Give the preparation type.
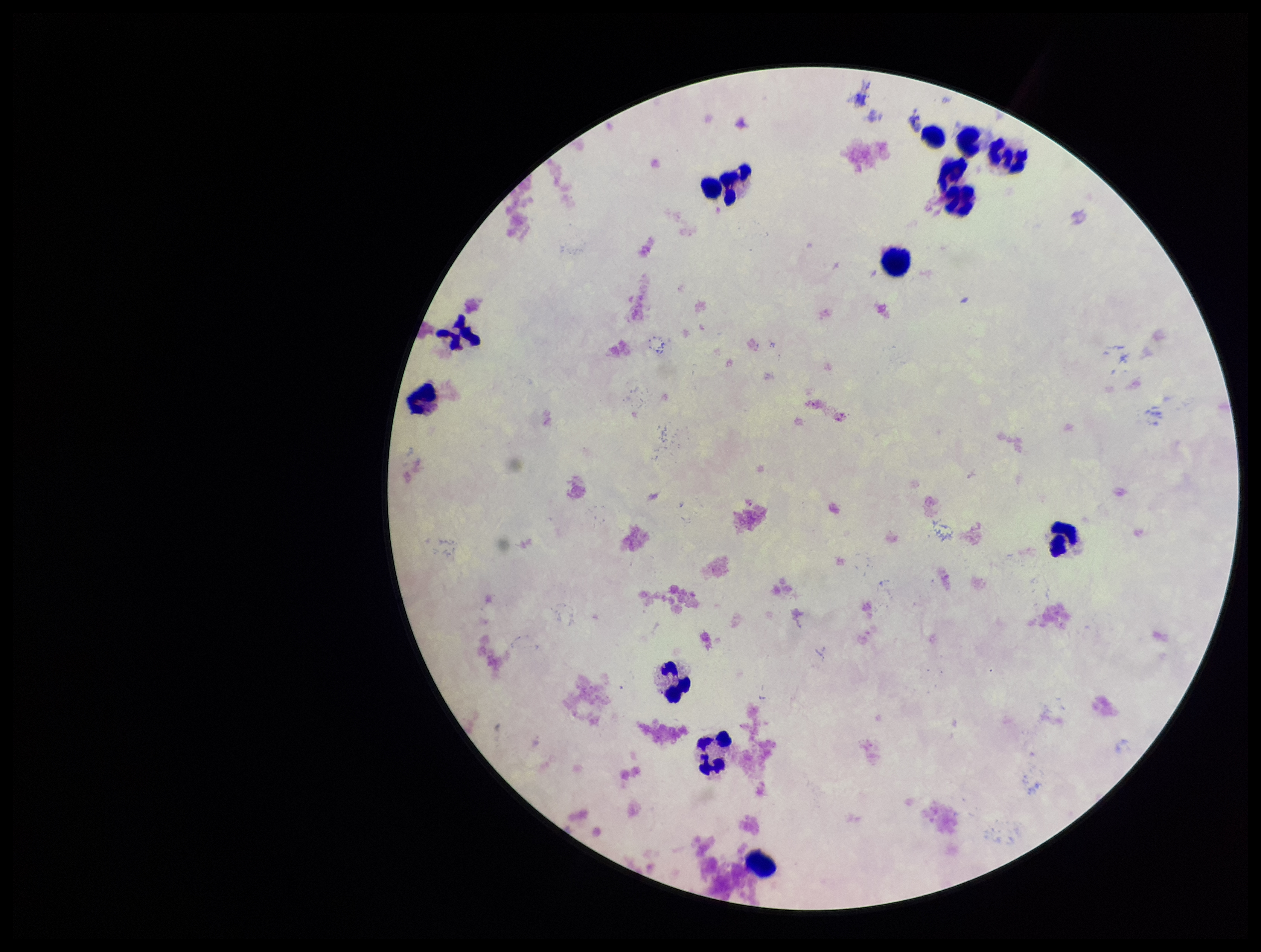

It is a thick blood smear.

Leukocyte count: 12. Patient malaria status: negative. Plasmodium parasites: none detected. Stained with Giemsa. Image is 1261×952 pixels. Single field of view. Photographed through the microscope eyepiece with a smartphone camera. Parasite count: 0.